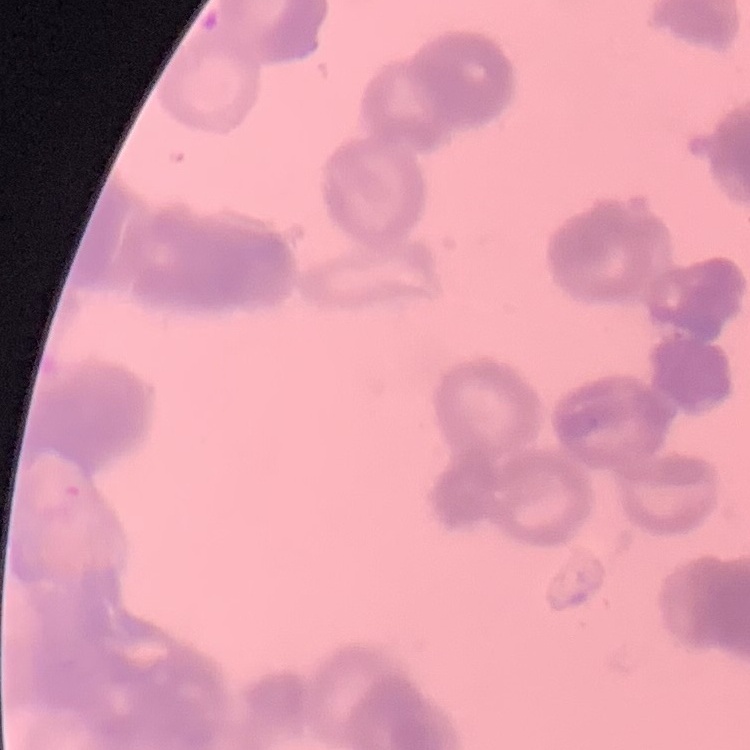

Summary:
  - Red blood cell morphology: rouleaux formation
  - Stain: Field's or Giemsa
  - Preparation: thin blood smear
  - Image type: square crop of a larger photomicrograph